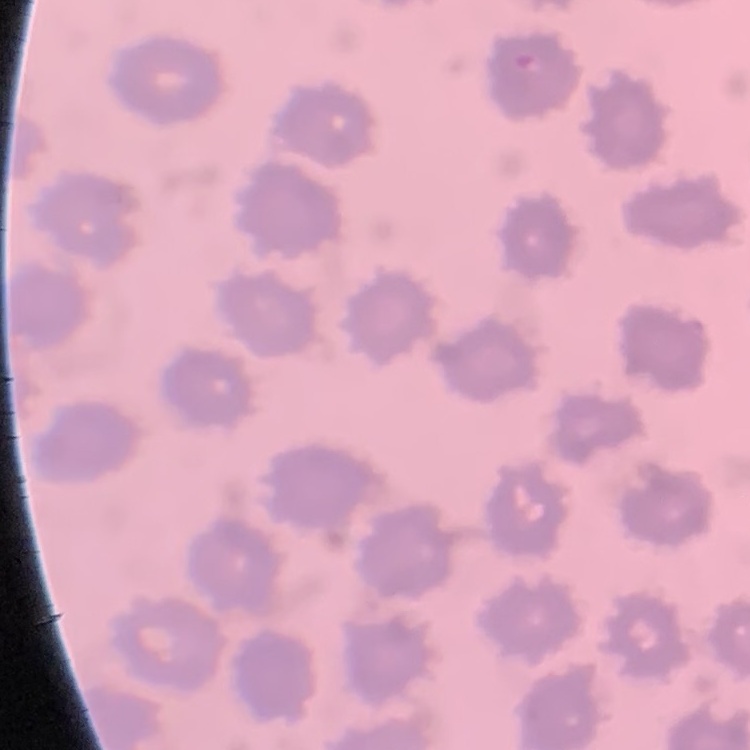

red blood cell morphology = no rouleaux formation
stain = Field's or Giemsa
image type = square crop of a larger photomicrograph
preparation = thin blood film